Classify this cell by malaria status.
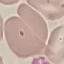
It is uninfected.

Thin blood smear. Acquired by smartphone through the microscope eyepiece. Giemsa-stained preparation. Cell patch, automatically extracted from a larger field of view and resized to 64 × 64 pixels.